Locate every malaria parasite and every leukocyte.
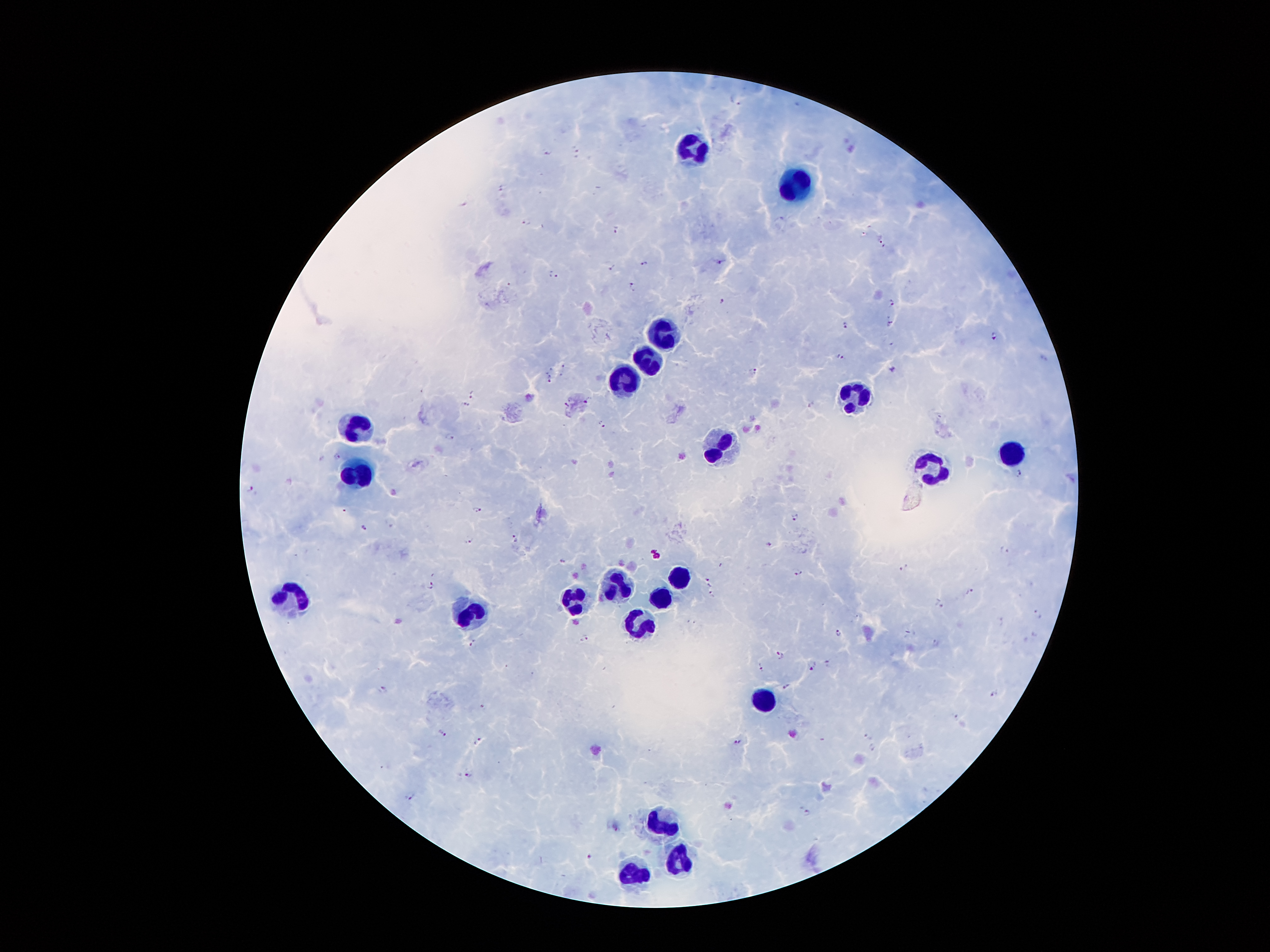
Approximate centers as [x, y] in pixels.
Malaria parasites: [736, 98], [576, 151], [547, 154], [501, 188], [525, 221], [616, 228], [879, 238], [719, 262], [644, 263], [612, 267], [553, 273], [632, 284], [723, 301], [891, 302], [891, 320], [845, 325], [994, 335], [840, 356], [563, 365], [891, 368], [754, 371], [549, 378], [471, 393], [588, 399], [567, 403], [466, 404], [601, 422], [449, 436], [337, 455], [336, 457], [1019, 471], [249, 487], [477, 509], [794, 517], [364, 528], [515, 538], [469, 541], [770, 543], [1005, 549], [561, 561], [904, 567], [797, 572], [709, 581], [430, 584], [968, 590], [712, 595], [940, 603], [1037, 614], [1000, 619], [840, 632], [584, 638], [936, 643], [473, 644], [779, 655], [826, 662], [760, 665], [811, 665], [786, 686], [383, 689], [993, 695], [956, 716], [443, 734], [868, 734], [477, 740], [738, 742], [871, 748], [468, 772], [409, 797], [805, 812], [590, 856].
Leukocytes: [694, 150], [795, 187], [664, 335], [648, 362], [626, 379], [855, 397], [360, 426], [724, 447], [1011, 450], [933, 468], [360, 476], [680, 577], [614, 582], [661, 595], [289, 596], [296, 598], [576, 598], [472, 614], [469, 616], [637, 623], [766, 701], [661, 826], [675, 860], [630, 875].

{
  "capture": "smartphone camera through the microscope eyepiece",
  "field_of_view": "one from this slide",
  "stain": "Giemsa",
  "patient_malaria_status": "positive for Plasmodium falciparum",
  "magnification": "100x",
  "preparation": "thick blood smear",
  "image_size": "1270×952 pixels"
}